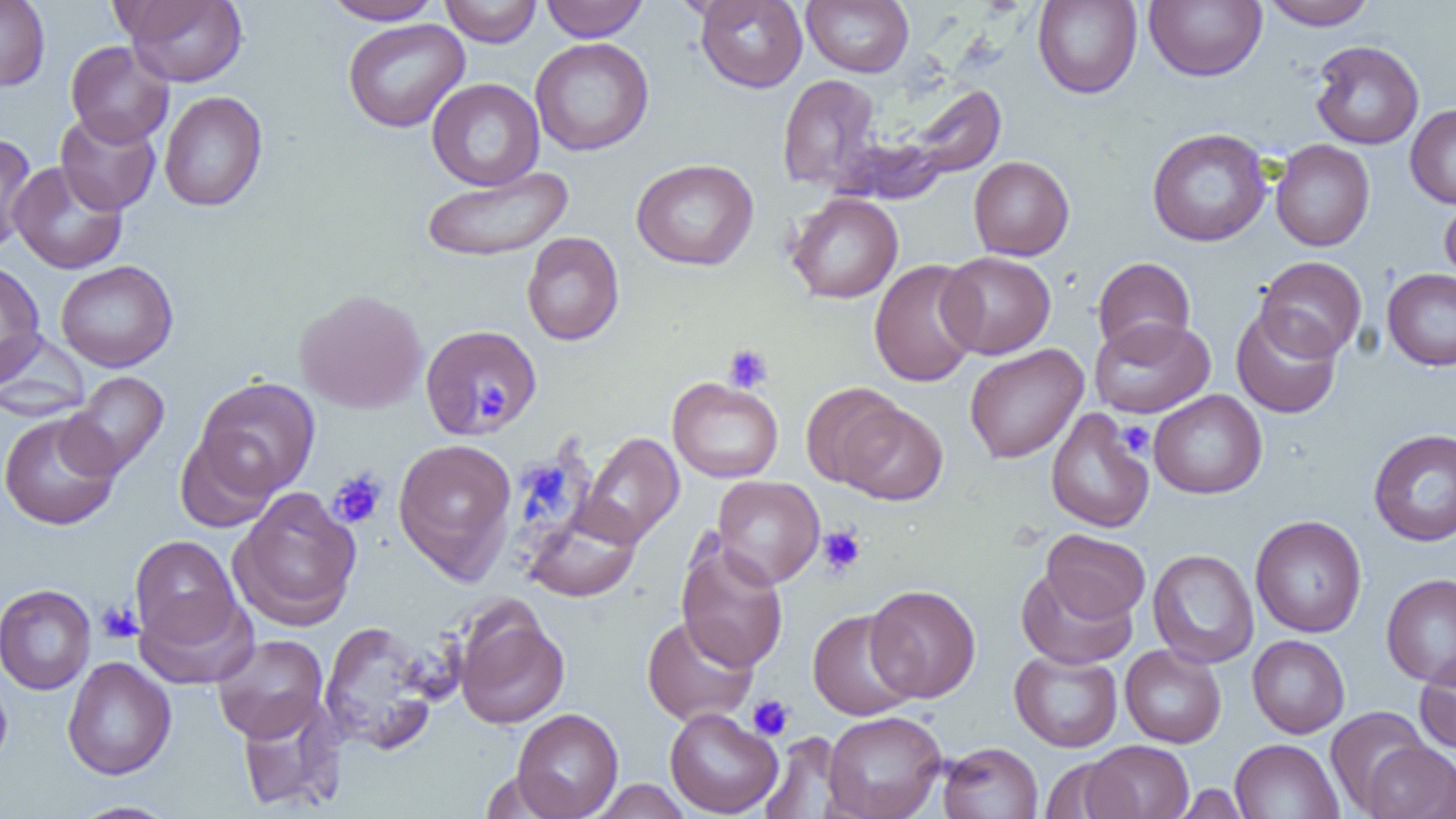
Approximate bounding boxes as (x1,y1)-(x2,y2) corner pairs in pixels. Platelet locations: (723,343)-(774,393), (475,385)-(507,416), (1118,420)-(1154,459), (327,469)-(387,529), (817,526)-(865,576), (96,600)-(142,643), (747,694)-(794,741). Uninfected red blood cell locations: (0,0)-(50,91), (120,0)-(248,86), (322,0)-(444,24), (440,0)-(542,47), (541,0)-(649,42), (694,0)-(808,92), (802,0)-(914,77), (1032,0)-(1142,99), (1144,0)-(1267,82), (1261,0)-(1377,30), (342,18)-(470,133), (530,37)-(654,156), (1310,40)-(1424,149), (65,41)-(174,147), (776,74)-(885,193), (427,78)-(544,190), (903,84)-(1006,182), (159,91)-(268,211), (1405,104)-(1456,208), (55,109)-(161,215), (1147,127)-(1272,246), (0,133)-(37,254), (1271,139)-(1375,251), (968,156)-(1074,260), (631,158)-(759,271), (9,161)-(127,274), (420,166)-(573,263), (786,193)-(903,304), (1440,196)-(1456,285), (522,231)-(624,346), (938,251)-(1056,359), (1255,256)-(1367,361), (1092,257)-(1196,356), (0,260)-(46,383), (55,260)-(178,372), (868,260)-(983,387), (1382,268)-(1456,371), (295,288)-(428,414), (1231,307)-(1342,418), (1089,316)-(1215,418), (419,324)-(543,439), (0,331)-(91,421), (964,344)-(1088,463), (62,371)-(169,479), (195,377)-(320,496), (668,377)-(783,483), (801,382)-(907,488), (1148,390)-(1267,499), (838,402)-(948,506), (1045,408)-(1154,533), (0,412)-(122,530), (1368,428)-(1456,547), (175,432)-(278,532), (579,432)-(683,546), (393,438)-(517,582), (711,475)-(824,588), (229,487)-(361,630), (524,507)-(642,602), (1250,515)-(1367,638), (1041,529)-(1150,623), (130,535)-(241,645), (676,541)-(789,671), (1147,549)-(1259,668), (1016,566)-(1137,669), (1381,573)-(1456,687), (0,584)-(95,695), (865,584)-(981,702), (134,590)-(258,690), (454,604)-(569,729), (807,609)-(920,720), (642,614)-(759,726), (319,621)-(441,753), (212,634)-(328,742), (1247,634)-(1349,738), (1120,644)-(1226,748), (1009,649)-(1123,752), (1415,654)-(1456,755), (62,656)-(176,780), (0,665)-(13,774), (237,696)-(346,813), (664,707)-(783,817), (1326,707)-(1431,813), (511,708)-(624,819), (822,710)-(947,819), (759,732)-(853,819), (1230,739)-(1343,819), (1082,740)-(1193,819), (937,742)-(1042,819), (1360,742)-(1456,819), (1040,758)-(1133,818), (590,780)-(693,818), (1171,783)-(1249,818), (69,801)-(179,818). Slide-level diagnosis: no evidence of blood parasites. Image is 1456×819 pixels. One field of a larger specimen. Thin blood smear. 1000x magnification. Optical microscopy.